Report the malaria status.
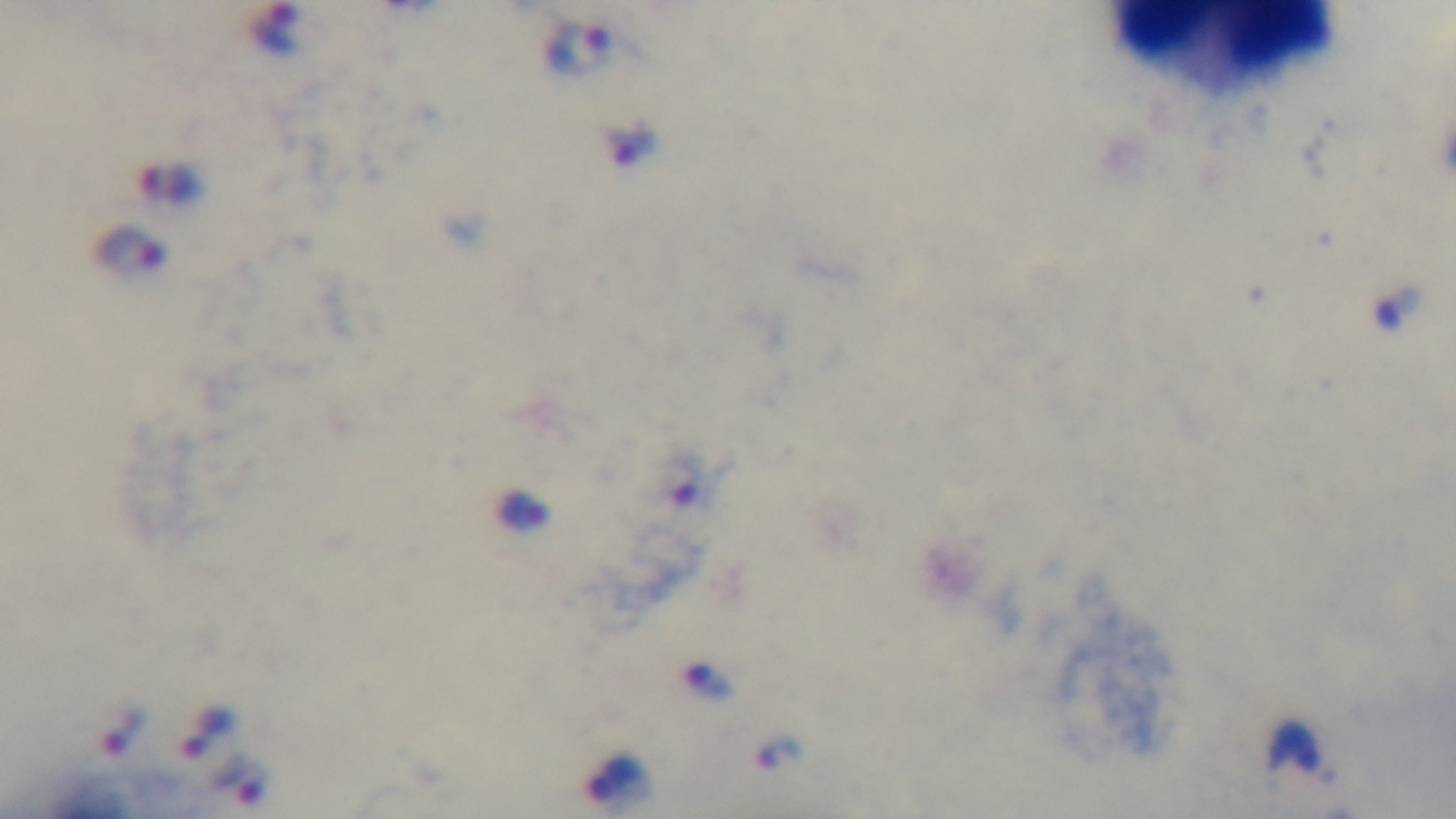
It is infected.

Giemsa stain. Preparation: thick blood film. Captured with a mounted 4K digital camera. 100x oil-immersion objective. Photomicrograph. One field from the slide.